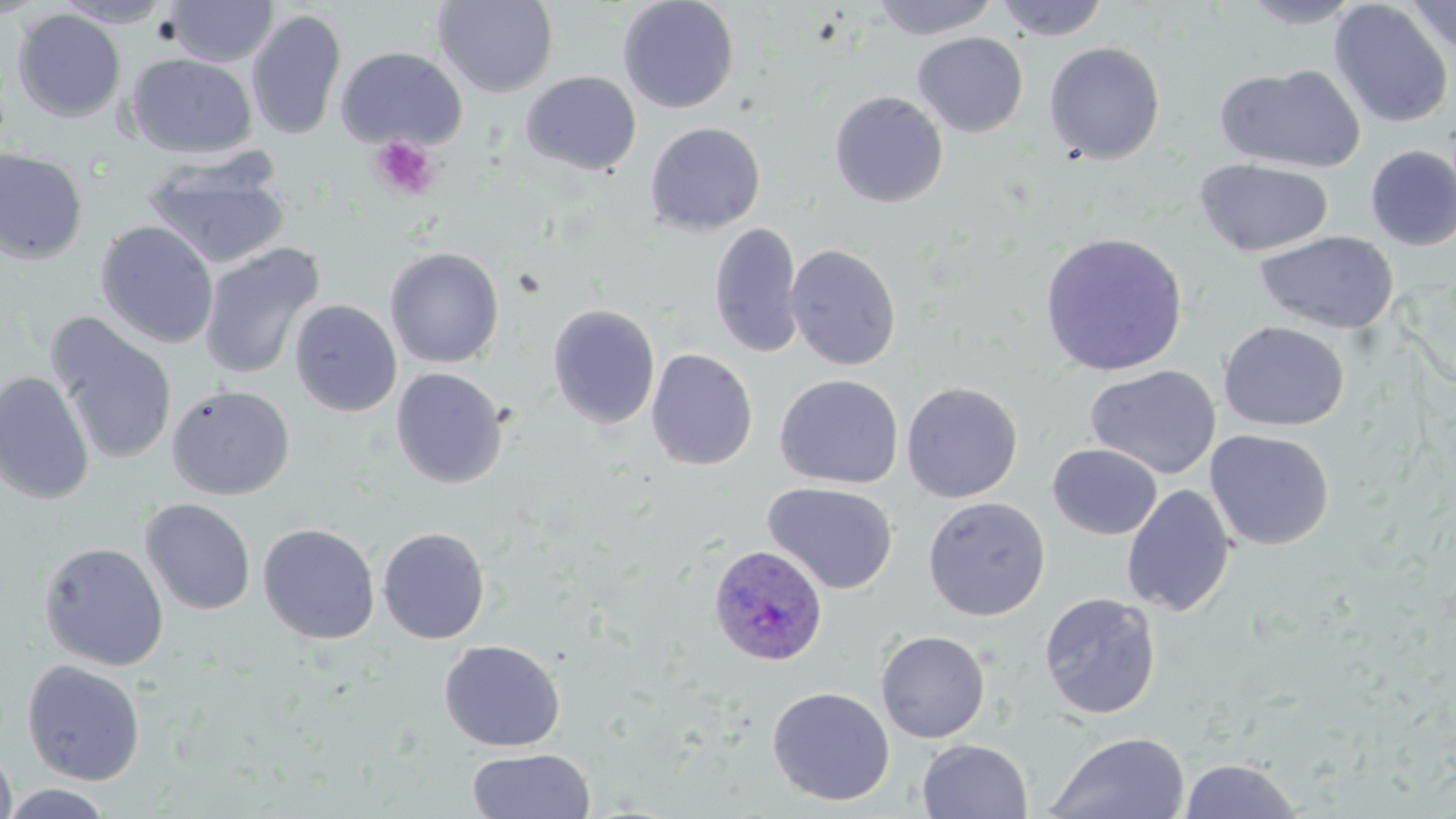 Approximate bounding boxes as (x1, y1, x2, y2) in pixels. Plasmodium ovale-infected red blood cell locations: (708, 543, 829, 666). Uninfected red blood cell locations: (50, 0, 178, 27), (618, 0, 740, 113), (871, 0, 1000, 39), (993, 0, 1111, 41), (1238, 0, 1366, 29), (1329, 0, 1454, 129), (1403, 0, 1456, 55), (166, 1, 278, 66), (433, 1, 559, 97), (13, 9, 126, 123), (246, 9, 347, 141), (912, 33, 1028, 137), (1044, 41, 1165, 165), (335, 46, 467, 150), (127, 53, 257, 158), (133, 55, 273, 264), (1214, 64, 1365, 173), (521, 71, 641, 175), (829, 90, 948, 207), (645, 122, 766, 235), (1364, 145, 1456, 250), (0, 148, 88, 264), (1194, 158, 1333, 257), (142, 162, 291, 270), (95, 221, 220, 348), (709, 222, 804, 358), (1039, 231, 1188, 376), (1255, 231, 1398, 334), (197, 243, 325, 380), (786, 243, 902, 370), (385, 247, 504, 368), (289, 299, 402, 417), (548, 304, 661, 429), (45, 313, 179, 465), (1218, 321, 1350, 432), (645, 348, 758, 471), (1085, 364, 1221, 480), (390, 367, 509, 489), (0, 371, 95, 504), (774, 374, 903, 489), (901, 381, 1023, 503), (166, 384, 295, 500), (1204, 428, 1335, 550), (1047, 443, 1162, 539), (763, 481, 898, 594), (1121, 484, 1236, 617), (922, 496, 1050, 620), (139, 498, 256, 615), (258, 523, 380, 644), (377, 526, 490, 644), (38, 541, 169, 670), (1039, 591, 1162, 720), (875, 629, 991, 743), (439, 639, 565, 752), (22, 660, 146, 785), (767, 686, 895, 806), (1045, 731, 1190, 819), (917, 738, 1033, 819), (0, 744, 17, 819), (466, 747, 595, 819), (1178, 757, 1303, 818), (1, 783, 115, 818). Platelet locations: (369, 135, 440, 201). Slide-level diagnosis: Plasmodium ovale. May-Grünwald-Giemsa-stained preparation. Image is 1456×819 pixels. Optical microscopy. One field of a larger specimen. Thin blood smear. Captured at 1000x magnification.